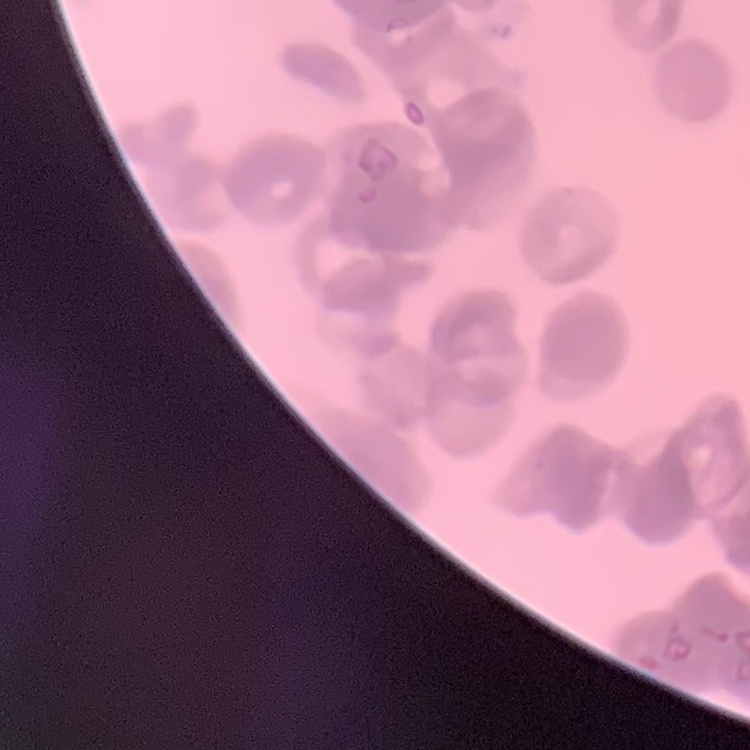

Summary:
  - Red blood cell morphology: rouleaux formation
  - Preparation: thin blood smear
  - Image type: square crop of a larger photomicrograph
  - Stain: Field's or Giemsa